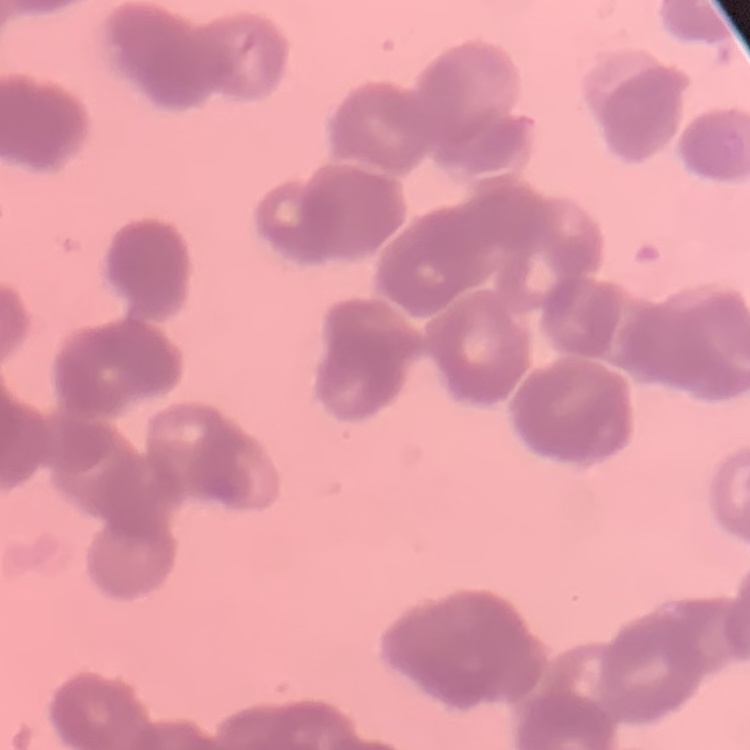

erythrocyte morphology = rouleaux formation
stain = Field's or Giemsa
image type = one tile cut from a larger photomicrograph
preparation = thin blood film